Classify this cell by malaria status.
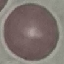

Uninfected.

Summary:
  - Image type: cell patch, automatically extracted from a larger field of view and resized to 64 × 64 pixels
  - Capture: smartphone through the microscope eyepiece
  - Stain: Giemsa
  - Preparation: thin blood smear